Give the position of every Plasmodium parasite.
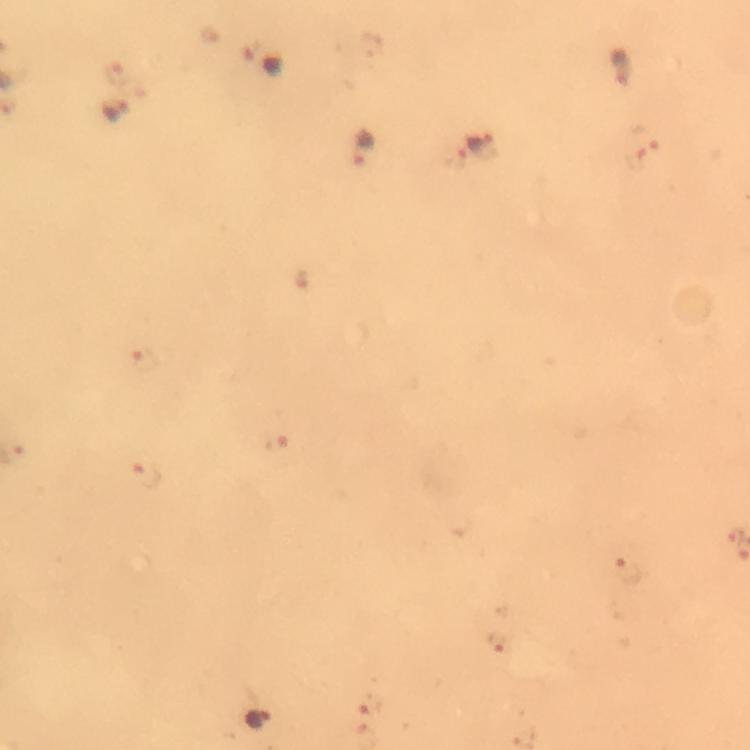
Approximate centers as (x, y) in pixels.
Plasmodium parasites: (264, 62), (624, 67), (115, 111), (480, 145), (364, 147), (146, 360), (276, 443), (146, 473), (255, 716).

Summary:
  - Immersion oil: used
  - Capture: smartphone camera through the microscope
  - Preparation: thick blood smear
  - Cropped from: one field of view
  - Magnification: 100x
  - Context: from a diagnostic examination for malaria
  - Image size: 750×750 pixels
  - Stain: Giemsa